Locate and identify every blood parasite.
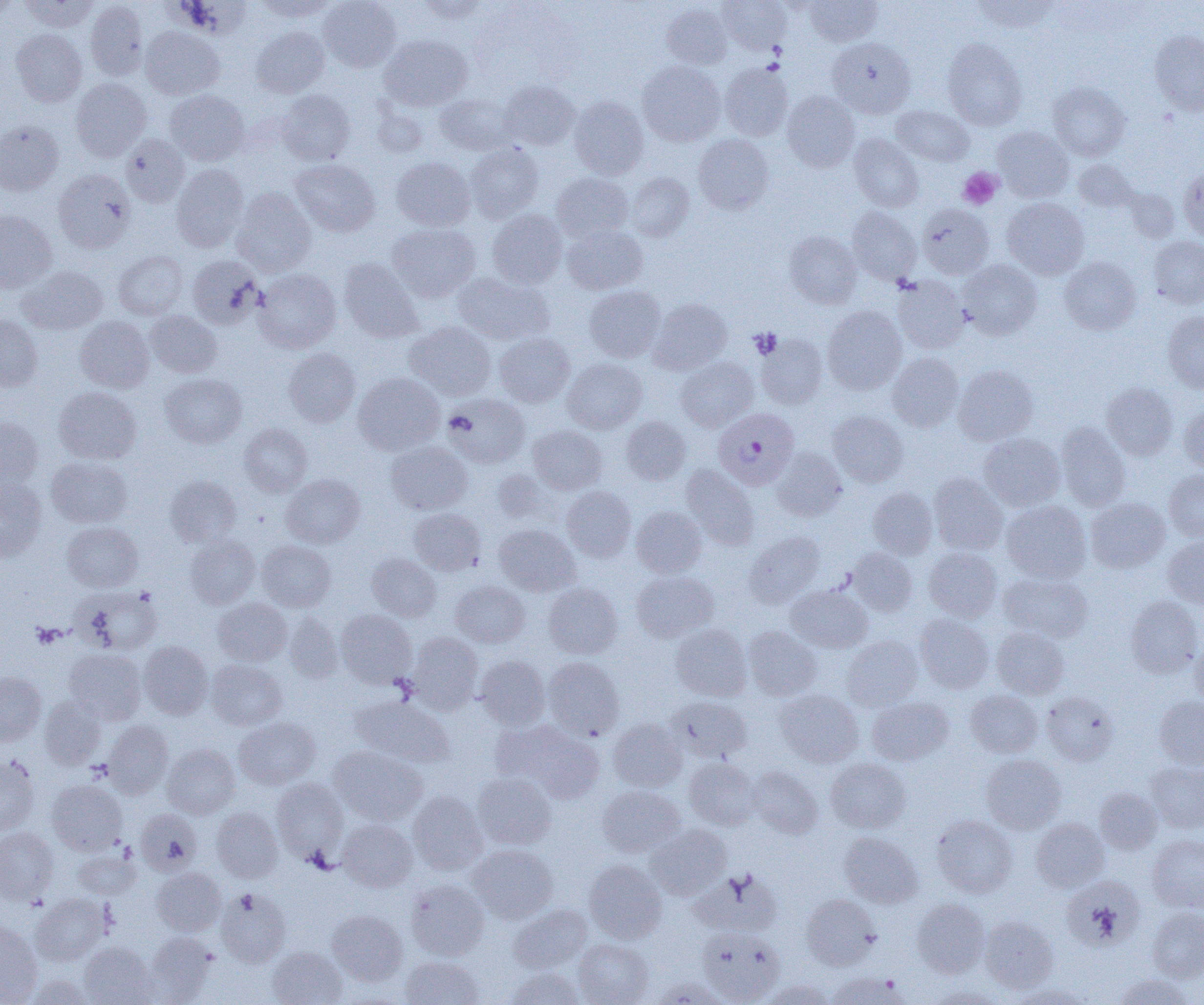
Approximate bounding boxes as named x1/y1/x2/y2 corners in pixels.
Plasmodium falciparum-infected red blood cells: (x1=713, y1=407, x2=800, y2=490).
No Plasmodium ovale, Plasmodium malariae, Plasmodium vivax, Babesia divergens, or Trypanosoma brucei observed.

{
  "slide_level_diagnosis": "Plasmodium falciparum",
  "uninfected_red_blood_cell_locations": "approximate bounding boxes as named x1/y1/x2/y2 corners in pixels: (x1=19, y1=0, x2=99, y2=32), (x1=253, y1=0, x2=338, y2=21), (x1=318, y1=0, x2=401, y2=72), (x1=415, y1=0, x2=492, y2=24), (x1=718, y1=0, x2=791, y2=54), (x1=805, y1=0, x2=882, y2=46), (x1=971, y1=0, x2=1059, y2=33), (x1=0, y1=1, x2=20, y2=19), (x1=85, y1=1, x2=148, y2=80), (x1=661, y1=3, x2=732, y2=69), (x1=141, y1=27, x2=224, y2=100), (x1=251, y1=27, x2=329, y2=98), (x1=11, y1=29, x2=87, y2=107), (x1=1149, y1=30, x2=1204, y2=116), (x1=379, y1=34, x2=473, y2=111), (x1=827, y1=37, x2=915, y2=119), (x1=942, y1=38, x2=1027, y2=130), (x1=637, y1=61, x2=725, y2=146), (x1=719, y1=62, x2=793, y2=141), (x1=71, y1=77, x2=152, y2=161), (x1=499, y1=81, x2=579, y2=150), (x1=1048, y1=82, x2=1130, y2=160), (x1=276, y1=89, x2=355, y2=166), (x1=165, y1=90, x2=249, y2=166), (x1=782, y1=91, x2=860, y2=172), (x1=435, y1=92, x2=516, y2=155), (x1=569, y1=96, x2=649, y2=179), (x1=891, y1=106, x2=974, y2=166), (x1=0, y1=120, x2=64, y2=196), (x1=993, y1=126, x2=1073, y2=202), (x1=121, y1=133, x2=190, y2=208), (x1=693, y1=134, x2=773, y2=215), (x1=849, y1=134, x2=924, y2=212), (x1=465, y1=143, x2=543, y2=223), (x1=391, y1=156, x2=475, y2=231), (x1=289, y1=159, x2=380, y2=237), (x1=1073, y1=160, x2=1138, y2=212), (x1=171, y1=164, x2=249, y2=252), (x1=1179, y1=167, x2=1204, y2=242), (x1=53, y1=168, x2=136, y2=254), (x1=626, y1=172, x2=694, y2=242), (x1=552, y1=173, x2=633, y2=242), (x1=232, y1=187, x2=316, y2=276), (x1=1123, y1=188, x2=1179, y2=243), (x1=1002, y1=198, x2=1089, y2=279), (x1=917, y1=203, x2=994, y2=279), (x1=847, y1=207, x2=921, y2=284), (x1=0, y1=210, x2=57, y2=293), (x1=487, y1=210, x2=567, y2=289), (x1=387, y1=223, x2=480, y2=303), (x1=562, y1=224, x2=647, y2=295), (x1=785, y1=231, x2=862, y2=308), (x1=1149, y1=236, x2=1204, y2=308), (x1=113, y1=251, x2=188, y2=320), (x1=187, y1=255, x2=264, y2=329), (x1=1059, y1=257, x2=1141, y2=335), (x1=339, y1=258, x2=423, y2=342), (x1=958, y1=260, x2=1042, y2=339), (x1=17, y1=266, x2=108, y2=335), (x1=252, y1=268, x2=341, y2=353), (x1=452, y1=273, x2=554, y2=345), (x1=893, y1=276, x2=969, y2=353), (x1=584, y1=286, x2=665, y2=362), (x1=649, y1=298, x2=731, y2=375), (x1=823, y1=306, x2=906, y2=395), (x1=146, y1=311, x2=222, y2=378), (x1=1163, y1=311, x2=1204, y2=393), (x1=0, y1=315, x2=43, y2=392), (x1=75, y1=316, x2=154, y2=393), (x1=404, y1=322, x2=496, y2=400), (x1=494, y1=332, x2=575, y2=407), (x1=756, y1=334, x2=827, y2=409), (x1=283, y1=347, x2=361, y2=428), (x1=887, y1=352, x2=964, y2=431), (x1=676, y1=357, x2=758, y2=431), (x1=562, y1=358, x2=647, y2=433), (x1=953, y1=365, x2=1038, y2=445), (x1=160, y1=373, x2=246, y2=448), (x1=353, y1=373, x2=445, y2=455), (x1=1102, y1=382, x2=1178, y2=460), (x1=54, y1=387, x2=142, y2=464), (x1=443, y1=393, x2=530, y2=468), (x1=1178, y1=403, x2=1204, y2=475), (x1=828, y1=410, x2=908, y2=487), (x1=621, y1=415, x2=690, y2=485), (x1=0, y1=417, x2=43, y2=490), (x1=239, y1=423, x2=313, y2=497), (x1=1056, y1=423, x2=1130, y2=511), (x1=528, y1=425, x2=607, y2=494), (x1=979, y1=433, x2=1065, y2=511), (x1=385, y1=441, x2=472, y2=515), (x1=772, y1=447, x2=847, y2=521), (x1=47, y1=456, x2=132, y2=528), (x1=681, y1=464, x2=759, y2=550), (x1=1164, y1=469, x2=1204, y2=542), (x1=281, y1=473, x2=365, y2=548), (x1=929, y1=473, x2=1008, y2=555), (x1=165, y1=475, x2=242, y2=547), (x1=0, y1=479, x2=47, y2=561), (x1=562, y1=486, x2=636, y2=562), (x1=868, y1=487, x2=938, y2=559), (x1=1086, y1=498, x2=1170, y2=573), (x1=1001, y1=500, x2=1091, y2=583), (x1=631, y1=506, x2=707, y2=577), (x1=408, y1=507, x2=486, y2=575), (x1=62, y1=522, x2=143, y2=592), (x1=494, y1=524, x2=580, y2=596), (x1=744, y1=531, x2=824, y2=607), (x1=185, y1=534, x2=260, y2=609), (x1=1163, y1=536, x2=1204, y2=608), (x1=257, y1=540, x2=336, y2=612), (x1=848, y1=547, x2=918, y2=616), (x1=923, y1=547, x2=1003, y2=622), (x1=367, y1=553, x2=441, y2=621), (x1=631, y1=570, x2=718, y2=642), (x1=999, y1=572, x2=1093, y2=643), (x1=450, y1=581, x2=530, y2=648), (x1=543, y1=583, x2=622, y2=658), (x1=786, y1=585, x2=872, y2=653), (x1=73, y1=586, x2=162, y2=655), (x1=1125, y1=596, x2=1203, y2=678), (x1=212, y1=598, x2=291, y2=666), (x1=336, y1=609, x2=416, y2=688), (x1=284, y1=612, x2=344, y2=683), (x1=915, y1=613, x2=993, y2=693), (x1=671, y1=623, x2=751, y2=701), (x1=744, y1=626, x2=821, y2=700), (x1=992, y1=627, x2=1069, y2=699), (x1=407, y1=632, x2=483, y2=714), (x1=841, y1=635, x2=923, y2=711), (x1=1191, y1=639, x2=1204, y2=708), (x1=138, y1=641, x2=213, y2=719), (x1=64, y1=649, x2=146, y2=724), (x1=475, y1=655, x2=550, y2=730), (x1=543, y1=656, x2=625, y2=740), (x1=206, y1=659, x2=287, y2=730), (x1=0, y1=672, x2=47, y2=746), (x1=775, y1=689, x2=863, y2=768), (x1=965, y1=690, x2=1042, y2=758), (x1=1041, y1=692, x2=1119, y2=765), (x1=350, y1=695, x2=455, y2=768), (x1=40, y1=696, x2=106, y2=769), (x1=666, y1=696, x2=753, y2=763), (x1=867, y1=696, x2=953, y2=765), (x1=1154, y1=696, x2=1204, y2=769), (x1=233, y1=716, x2=320, y2=790), (x1=608, y1=718, x2=687, y2=792), (x1=103, y1=720, x2=173, y2=799), (x1=496, y1=720, x2=605, y2=804), (x1=162, y1=743, x2=240, y2=819), (x1=328, y1=745, x2=427, y2=826), (x1=981, y1=754, x2=1066, y2=834), (x1=0, y1=755, x2=40, y2=836), (x1=684, y1=757, x2=761, y2=830), (x1=825, y1=759, x2=911, y2=833), (x1=1145, y1=761, x2=1204, y2=832), (x1=747, y1=766, x2=823, y2=838), (x1=472, y1=772, x2=557, y2=850), (x1=272, y1=778, x2=348, y2=862), (x1=47, y1=779, x2=127, y2=854), (x1=597, y1=785, x2=685, y2=858), (x1=1094, y1=788, x2=1161, y2=854), (x1=407, y1=790, x2=488, y2=875), (x1=212, y1=806, x2=283, y2=882), (x1=136, y1=809, x2=202, y2=875), (x1=931, y1=815, x2=1017, y2=897), (x1=1031, y1=818, x2=1109, y2=892), (x1=337, y1=819, x2=417, y2=892), (x1=645, y1=823, x2=732, y2=899), (x1=0, y1=828, x2=59, y2=904), (x1=838, y1=832, x2=923, y2=908), (x1=1147, y1=834, x2=1204, y2=913), (x1=468, y1=844, x2=559, y2=924), (x1=72, y1=846, x2=141, y2=899), (x1=584, y1=859, x2=667, y2=943), (x1=692, y1=866, x2=783, y2=936), (x1=152, y1=868, x2=226, y2=936), (x1=1061, y1=875, x2=1144, y2=951), (x1=406, y1=878, x2=489, y2=960), (x1=216, y1=888, x2=291, y2=967), (x1=802, y1=893, x2=881, y2=970), (x1=31, y1=894, x2=109, y2=965), (x1=912, y1=899, x2=990, y2=978), (x1=509, y1=904, x2=591, y2=973), (x1=1147, y1=907, x2=1204, y2=982), (x1=327, y1=910, x2=407, y2=986), (x1=979, y1=915, x2=1059, y2=993), (x1=0, y1=921, x2=43, y2=1005), (x1=697, y1=926, x2=785, y2=1004), (x1=145, y1=931, x2=217, y2=1003), (x1=574, y1=938, x2=654, y2=1005), (x1=79, y1=941, x2=157, y2=1005), (x1=267, y1=946, x2=347, y2=1005), (x1=400, y1=955, x2=485, y2=1004), (x1=504, y1=967, x2=584, y2=1005), (x1=827, y1=971, x2=911, y2=1005), (x1=1113, y1=973, x2=1194, y2=1005), (x1=26, y1=974, x2=97, y2=1004), (x1=651, y1=975, x2=731, y2=1005), (x1=761, y1=979, x2=836, y2=1005), (x1=1009, y1=984, x2=1093, y2=1005), (x1=927, y1=986, x2=1006, y2=1004)",
  "platelet_locations": "approximate bounding boxes as named x1/y1/x2/y2 corners in pixels: (x1=958, y1=167, x2=1002, y2=209), (x1=750, y1=328, x2=781, y2=358), (x1=31, y1=623, x2=63, y2=648)",
  "modality": "light microscopy",
  "image_size": "1204×1005 pixels",
  "field_of_view": "single",
  "preparation": "thin blood film",
  "magnification": "1000x"
}